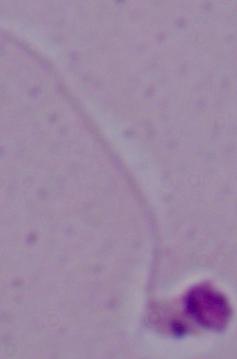

Photomicrograph. 1000x magnification. A Leishmania parasite is seen.